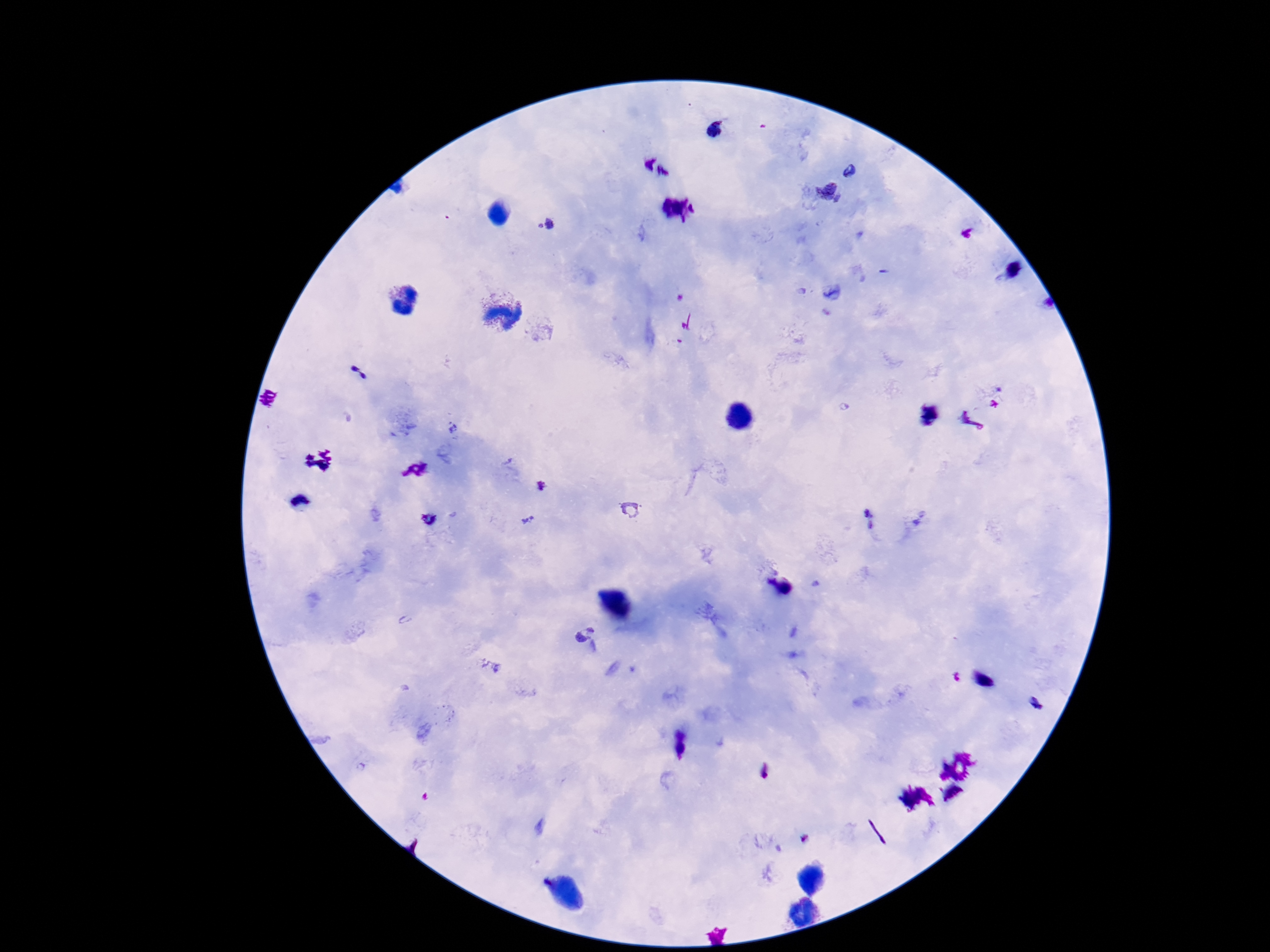
{
  "patient_malaria_status": "infected",
  "plasmodium_parasite_locations": "approximate centers as {x, y} in pixels: {715, 130}, {851, 173}, {827, 191}, {544, 225}, {454, 428}, {542, 486}, {632, 509}, {430, 518}, {526, 520}, {869, 520}, {581, 634}",
  "stain": "Giemsa",
  "field_of_view": "one from this slide",
  "image_size": "1270×952 pixels",
  "preparation": "thick blood smear",
  "magnification": "100x",
  "capture": "smartphone camera through the microscope eyepiece"
}